Locate every uninfected red blood cell.
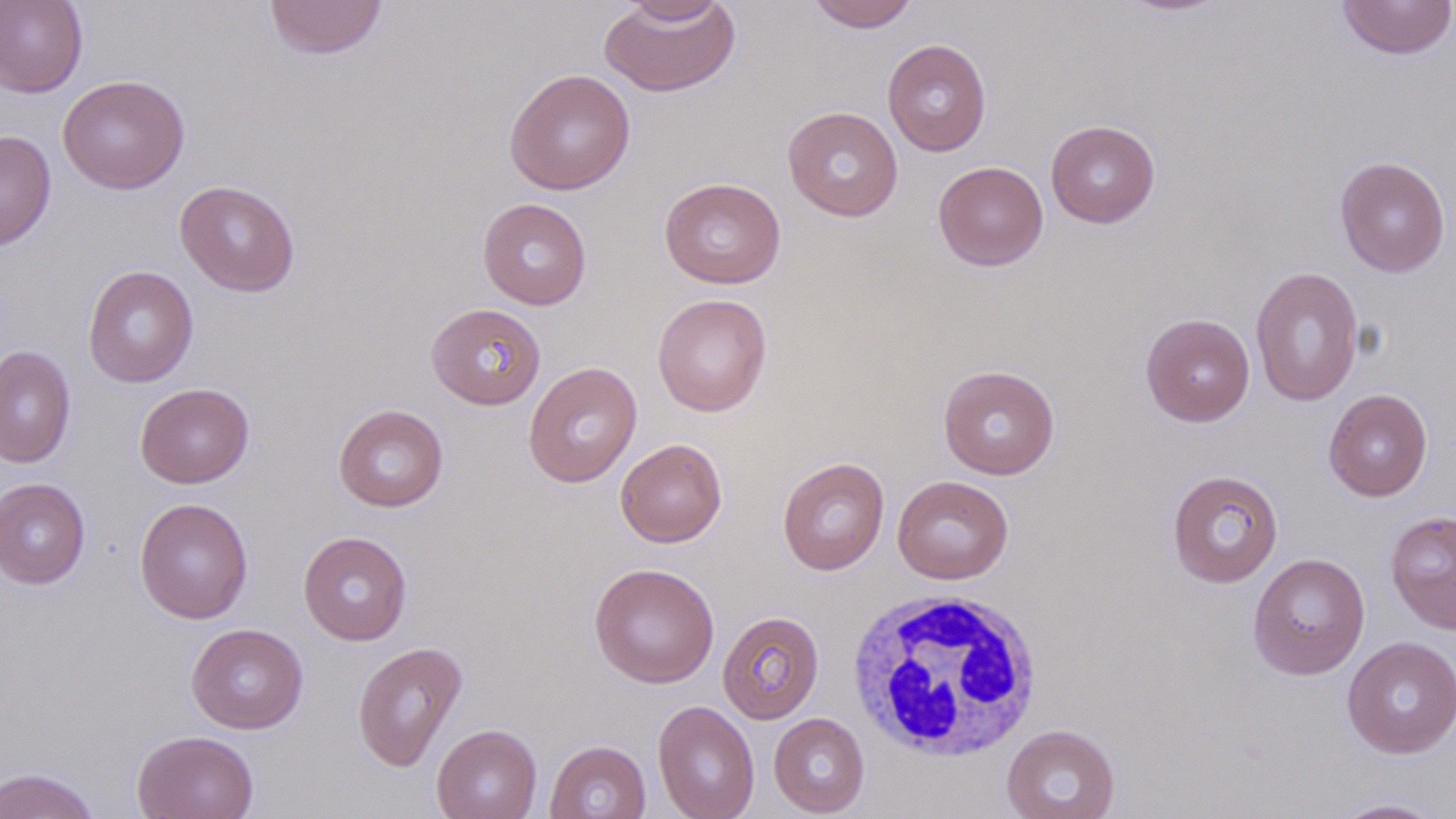
Approximate bounding boxes as [x1, y1, x2, y2] in pixels.
Uninfected red blood cells: [0, 0, 88, 97], [264, 0, 388, 60], [598, 0, 741, 98], [611, 0, 736, 24], [806, 0, 920, 32], [1115, 0, 1233, 17], [1337, 0, 1456, 60], [882, 38, 992, 156], [504, 68, 636, 195], [57, 74, 190, 194], [782, 106, 903, 222], [1045, 119, 1160, 228], [0, 129, 56, 251], [1335, 156, 1450, 277], [933, 161, 1048, 271], [659, 177, 786, 289], [175, 180, 300, 296], [477, 197, 592, 310], [83, 265, 198, 388], [1250, 266, 1364, 407], [652, 293, 772, 417], [426, 303, 545, 409], [1140, 313, 1255, 427], [0, 345, 76, 468], [523, 362, 642, 488], [938, 364, 1060, 479], [135, 383, 254, 488], [1323, 388, 1433, 501], [333, 404, 449, 511], [615, 438, 727, 547], [777, 457, 890, 575], [1167, 469, 1284, 588], [892, 475, 1014, 584], [0, 478, 90, 589], [134, 497, 253, 624], [1386, 509, 1456, 633], [298, 531, 412, 645], [1248, 552, 1370, 680], [588, 562, 720, 688], [717, 611, 824, 724], [186, 623, 308, 734], [1342, 636, 1456, 758], [352, 640, 468, 773], [653, 700, 759, 819], [768, 712, 870, 817], [431, 724, 542, 819], [1001, 724, 1120, 819], [132, 730, 259, 819], [545, 740, 651, 819], [1, 767, 101, 818], [1328, 797, 1450, 818].

Summary:
  - White blood cell locations: [845, 587, 1044, 761]
  - Slide-level diagnosis: negative for blood parasites
  - Preparation: thin blood smear
  - Stain: May-Grünwald-Giemsa
  - Modality: optical microscopy
  - Magnification: 1000x
  - Field of view: single
  - Image size: 1456×819 pixels